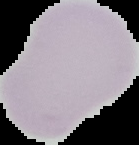
Summary:
  - Preparation: thin blood film
  - Image size: 139×145 pixels
  - Malaria status: uninfected
  - Image type: segmented cell region on a black background